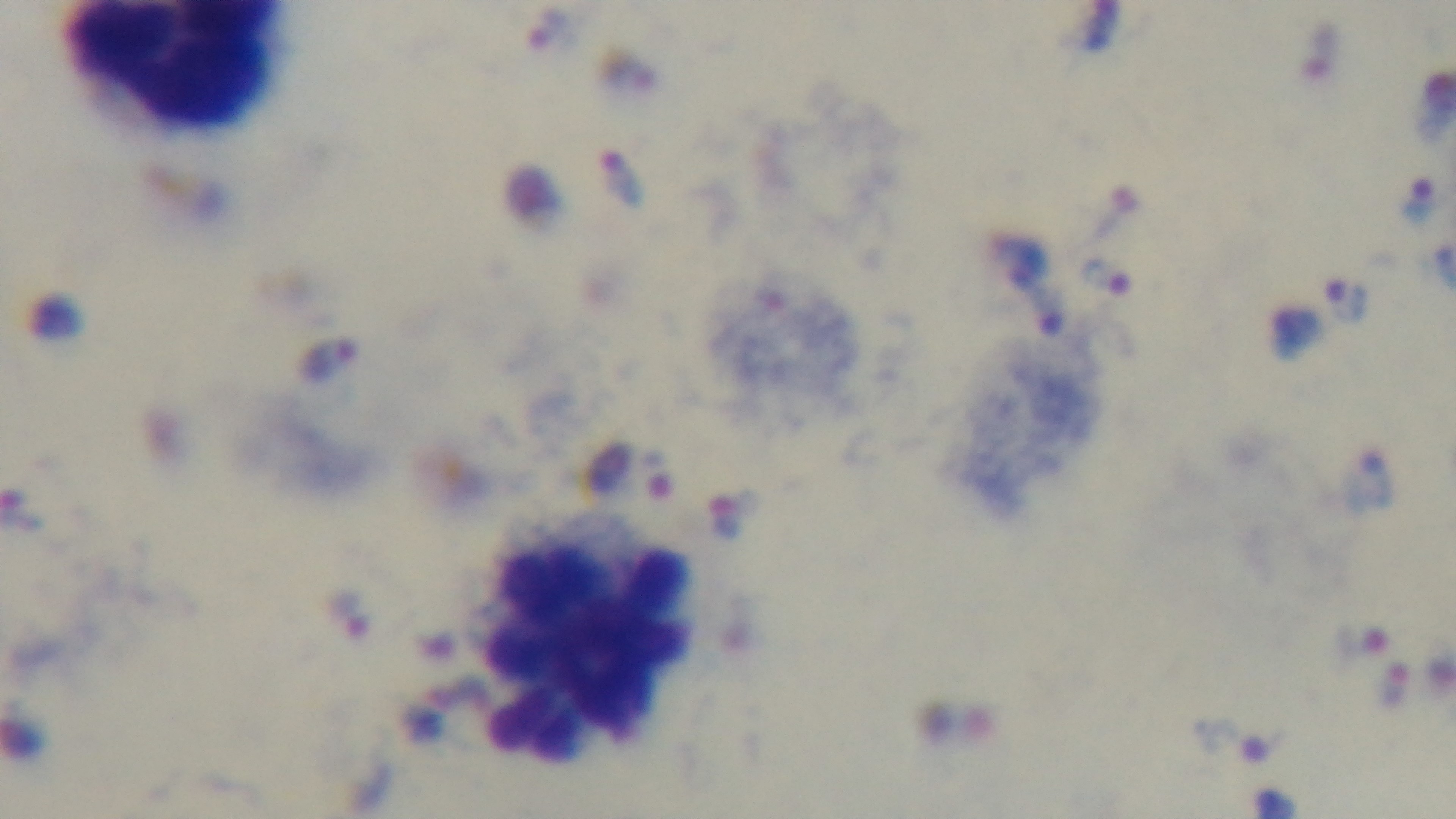
Summary:
  - Objective: 100x oil immersion
  - Capture: mounted 4K digital camera
  - Field of view: single
  - Stain: Giemsa
  - Malaria status: positive
  - Preparation: thick blood film
  - Modality: light microscopy